Classify this cell by malaria status.
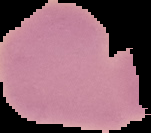

It is uninfected.

Image is 151×133 pixels. From a thin blood film. The area outside the segmented cell region is set to black.